Classify this cell by malaria status.
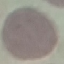
It is uninfected.

{
  "preparation": "thin blood film",
  "image_type": "cell patch, automatically extracted from a larger field of view and resized to 64 × 64 pixels",
  "capture": "smartphone through the microscope eyepiece",
  "stain": "Giemsa"
}